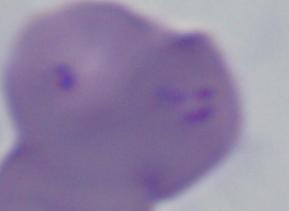
Summary:
  - Magnification: 1000x
  - Modality: micrograph
  - Identification: Babesia